Outline each Plasmodium vivax-infected red blood cell.
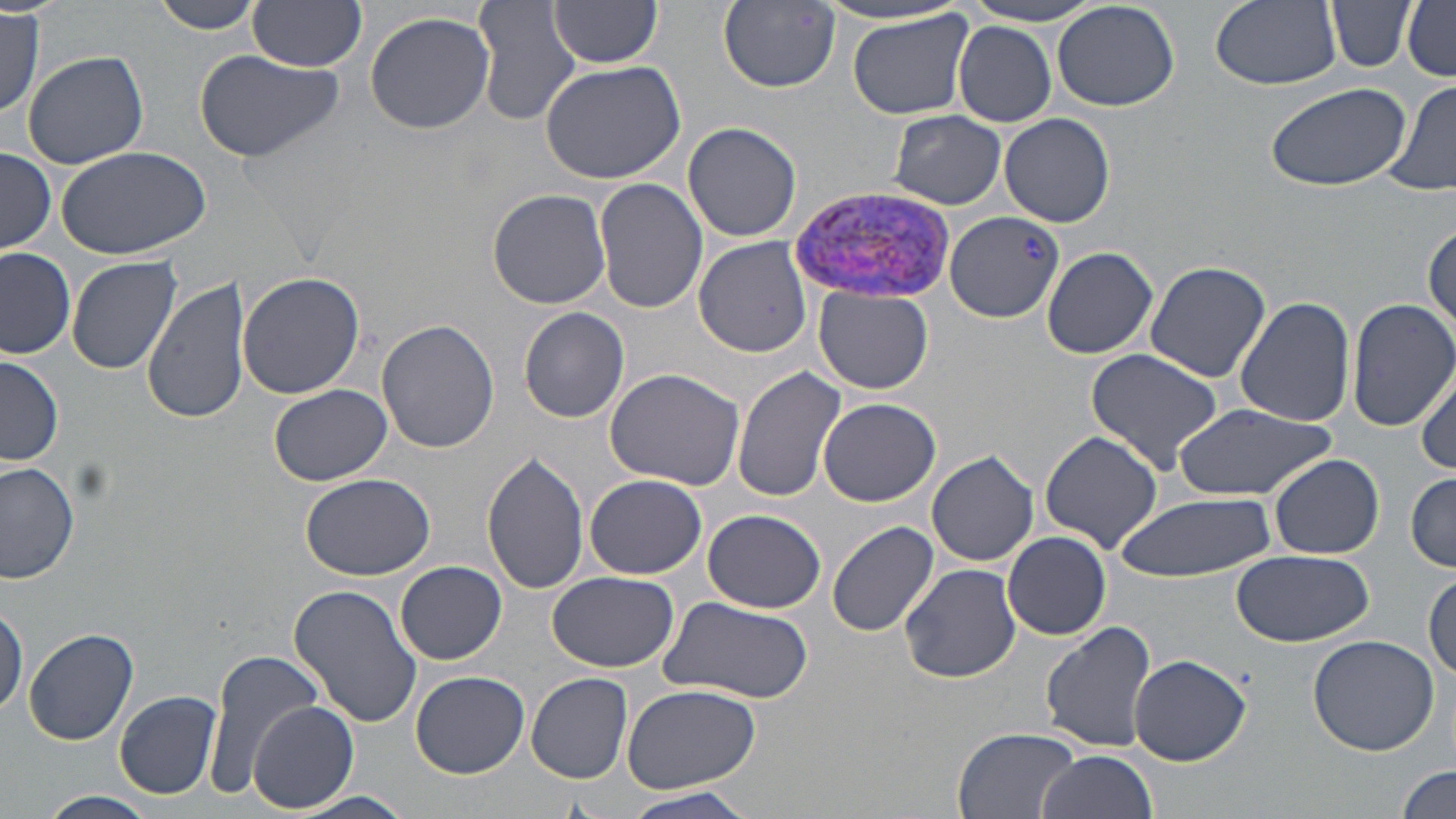
Approximate bounding boxes as [x1, y1, x2, y2] in pixels.
Plasmodium vivax-infected red blood cells: [788, 184, 959, 304].

Summary:
  - Uninfected red blood cell locations: [148, 0, 266, 34], [249, 0, 368, 71], [719, 0, 841, 91], [1208, 0, 1343, 92], [1326, 0, 1415, 72], [547, 1, 664, 68], [958, 1, 1111, 26], [472, 2, 580, 128], [1401, 2, 1456, 80], [811, 3, 972, 28], [1053, 3, 1181, 112], [846, 9, 975, 121], [1, 10, 46, 119], [365, 10, 496, 134], [953, 22, 1057, 125], [21, 48, 149, 170], [191, 48, 344, 164], [539, 58, 687, 186], [1385, 80, 1456, 199], [1263, 81, 1410, 194], [888, 111, 1007, 208], [1000, 112, 1115, 228], [682, 121, 802, 243], [53, 143, 212, 257], [1, 147, 56, 253], [595, 177, 709, 315], [488, 189, 612, 309], [945, 212, 1064, 322], [1425, 221, 1455, 338], [693, 235, 811, 356], [1040, 245, 1158, 359], [0, 249, 77, 360], [66, 255, 182, 374], [1144, 261, 1273, 385], [235, 272, 366, 399], [144, 275, 252, 426], [815, 287, 933, 395], [1235, 296, 1358, 427], [1347, 297, 1456, 431], [519, 307, 630, 423], [377, 319, 501, 454], [1084, 348, 1225, 473], [1, 354, 63, 468], [1052, 362, 1196, 527], [1414, 364, 1456, 474], [731, 366, 845, 502], [604, 368, 745, 490], [266, 384, 394, 487], [818, 398, 942, 508], [1171, 404, 1334, 501], [1039, 431, 1163, 551], [926, 449, 1039, 568], [482, 451, 591, 594], [1268, 454, 1385, 560], [0, 461, 79, 584], [1406, 472, 1456, 570], [300, 473, 436, 581], [586, 474, 707, 579], [1113, 490, 1278, 581], [702, 509, 826, 614], [827, 520, 940, 637], [1002, 530, 1111, 640], [1231, 549, 1374, 647], [397, 561, 506, 664], [899, 563, 1023, 682], [1425, 570, 1456, 681], [547, 571, 679, 672], [288, 583, 424, 731], [0, 596, 27, 719], [658, 596, 816, 705], [1040, 620, 1159, 754], [24, 628, 140, 747], [1308, 634, 1442, 755], [202, 649, 330, 800], [1130, 654, 1251, 766], [411, 670, 529, 778], [527, 672, 632, 783], [620, 683, 763, 792], [117, 692, 221, 799], [249, 700, 359, 813], [950, 729, 1086, 817], [1036, 750, 1157, 819], [1396, 766, 1455, 819], [618, 787, 759, 817], [42, 790, 159, 817], [291, 792, 412, 819]
  - Slide-level diagnosis: Plasmodium vivax
  - Magnification: 1000x
  - Modality: optical microscopy
  - Preparation: thin blood film
  - Field of view: one of a larger specimen
  - Image size: 1456×819 pixels
  - Stain: May-Grünwald-Giemsa